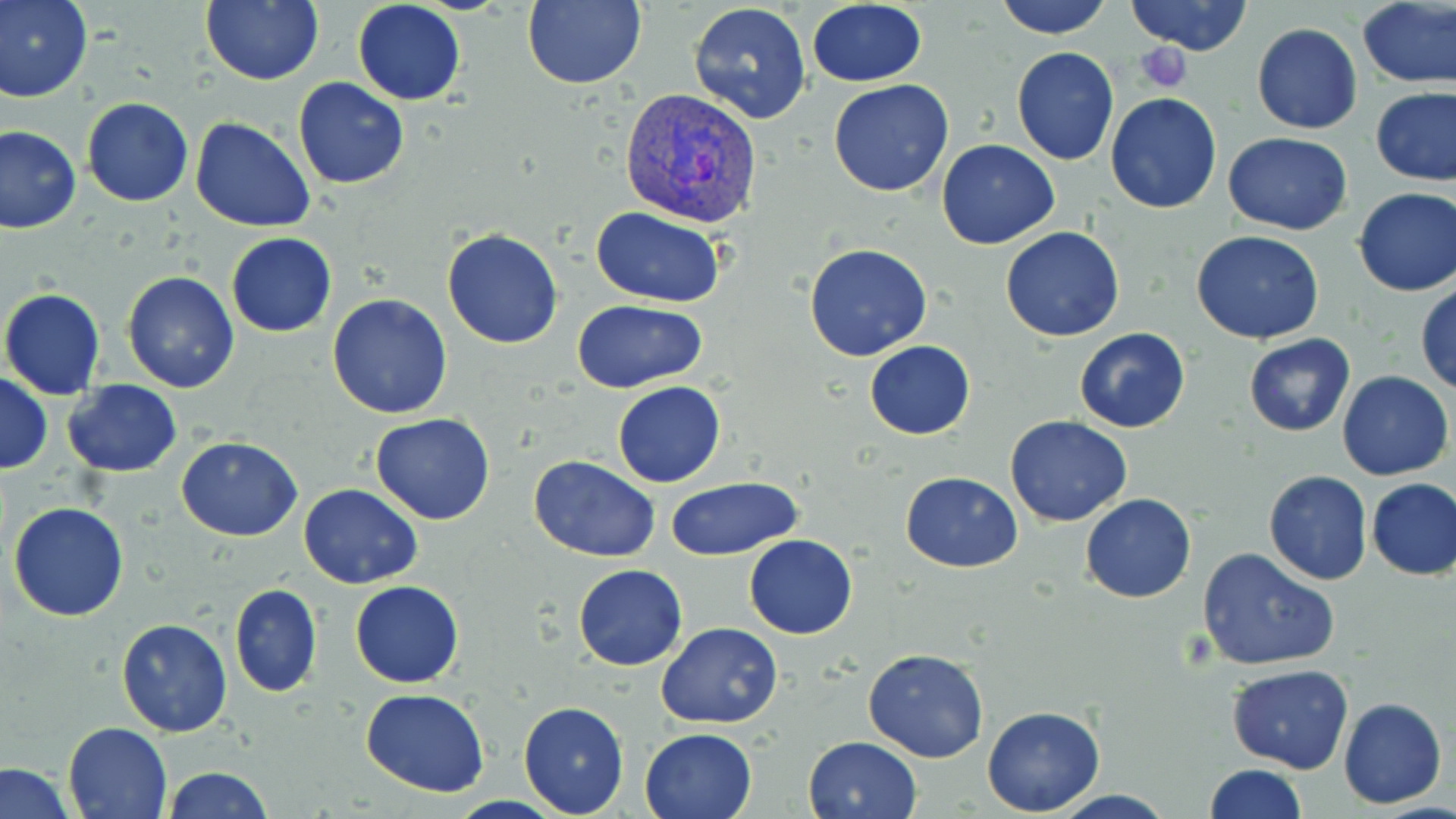

Summary:
  - Coordinate format: approximate bounding boxes as (x1,y1)-(x2,y2) corner pairs in pixels
  - Plasmodium vivax-infected red blood cell locations: (618,86)-(765,230)
  - Uninfected red blood cell locations: (0,0)-(93,103), (203,0)-(325,85), (352,0)-(466,105), (523,0)-(647,90), (994,0)-(1112,39), (1125,0)-(1254,56), (806,1)-(926,86), (687,2)-(812,125), (1357,2)-(1456,88), (1251,23)-(1362,134), (1011,47)-(1120,165), (293,78)-(409,189), (828,78)-(954,197), (1371,87)-(1456,185), (1105,93)-(1223,213), (82,97)-(193,206), (190,116)-(317,233), (0,126)-(81,234), (1223,133)-(1351,235), (937,139)-(1060,250), (1353,188)-(1456,298), (591,208)-(729,309), (1000,227)-(1125,343), (441,228)-(564,348), (1191,230)-(1324,345), (226,232)-(337,337), (803,244)-(932,362), (120,272)-(240,394), (1415,285)-(1456,397), (1,288)-(107,399), (327,294)-(454,419), (574,300)-(707,393), (1074,327)-(1190,434), (1243,334)-(1356,437), (864,340)-(976,440), (1337,371)-(1453,480), (0,373)-(50,474), (61,380)-(182,476), (613,381)-(726,488), (369,414)-(496,526), (1005,415)-(1131,527), (176,435)-(301,541), (530,456)-(658,562), (1264,470)-(1372,585), (900,471)-(1022,573), (667,476)-(805,559), (1365,477)-(1456,580), (298,484)-(423,589), (1080,493)-(1196,603), (8,501)-(128,621), (743,534)-(857,639), (1197,546)-(1341,672), (573,564)-(688,670), (350,580)-(463,687), (229,583)-(323,699), (116,618)-(234,736), (656,621)-(783,729), (863,647)-(990,763), (1227,663)-(1354,774), (361,689)-(489,797), (1338,698)-(1446,808), (518,701)-(630,817), (982,705)-(1106,815), (63,721)-(173,818), (639,727)-(759,819), (803,735)-(921,819), (0,762)-(74,819), (1202,764)-(1307,819), (163,766)-(273,819)
  - Platelet locations: (1135,44)-(1193,92)
  - Slide-level diagnosis: Plasmodium vivax
  - Stain: May-Grünwald-Giemsa
  - Image size: 1456×819 pixels
  - Preparation: thin blood smear
  - Modality: optical microscopy
  - Field of view: single
  - Magnification: 1000x